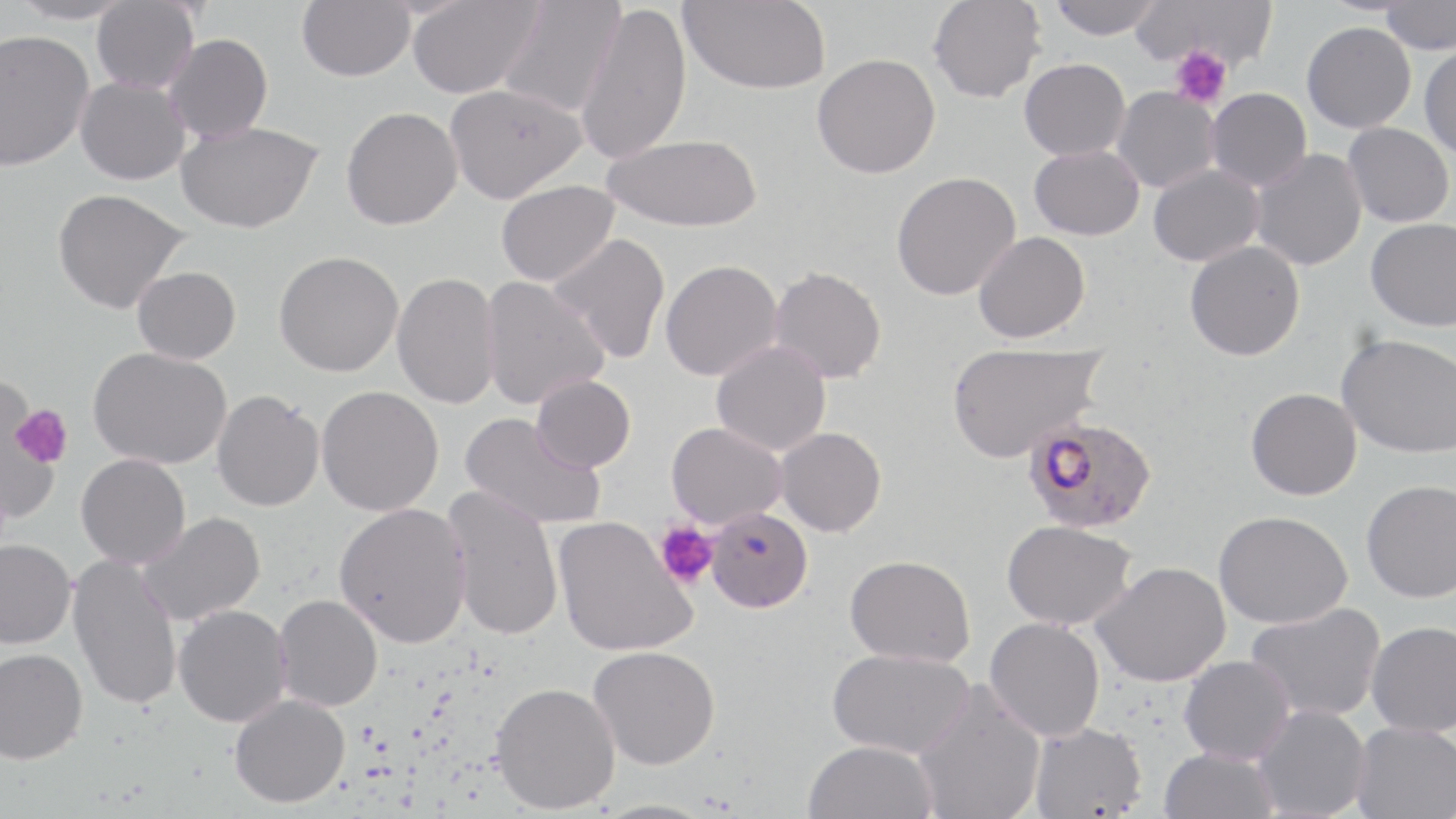
Approximate bounding boxes as named x1/y1/x2/y2 corners in pixels. Uninfected red blood cell locations: (x1=9, y1=0, x2=135, y2=25), (x1=297, y1=0, x2=414, y2=81), (x1=498, y1=0, x2=625, y2=117), (x1=680, y1=0, x2=830, y2=94), (x1=928, y1=0, x2=1045, y2=103), (x1=1047, y1=0, x2=1163, y2=40), (x1=1132, y1=0, x2=1276, y2=68), (x1=1381, y1=0, x2=1456, y2=54), (x1=91, y1=1, x2=199, y2=94), (x1=407, y1=1, x2=542, y2=98), (x1=575, y1=2, x2=691, y2=166), (x1=1301, y1=21, x2=1416, y2=133), (x1=0, y1=29, x2=94, y2=171), (x1=163, y1=34, x2=273, y2=142), (x1=1419, y1=44, x2=1456, y2=160), (x1=811, y1=53, x2=940, y2=179), (x1=1019, y1=58, x2=1130, y2=161), (x1=75, y1=76, x2=190, y2=185), (x1=444, y1=83, x2=585, y2=203), (x1=1111, y1=86, x2=1220, y2=193), (x1=1206, y1=87, x2=1312, y2=191), (x1=341, y1=106, x2=462, y2=230), (x1=175, y1=120, x2=323, y2=233), (x1=1343, y1=122, x2=1454, y2=228), (x1=602, y1=133, x2=763, y2=232), (x1=1029, y1=145, x2=1144, y2=241), (x1=1249, y1=149, x2=1367, y2=271), (x1=1148, y1=164, x2=1264, y2=266), (x1=891, y1=171, x2=1020, y2=300), (x1=496, y1=180, x2=619, y2=286), (x1=52, y1=188, x2=190, y2=313), (x1=1366, y1=218, x2=1456, y2=331), (x1=973, y1=231, x2=1089, y2=343), (x1=548, y1=233, x2=670, y2=364), (x1=1184, y1=240, x2=1305, y2=361), (x1=274, y1=251, x2=403, y2=376), (x1=660, y1=259, x2=783, y2=381), (x1=132, y1=266, x2=240, y2=364), (x1=769, y1=266, x2=887, y2=383), (x1=392, y1=271, x2=501, y2=409), (x1=481, y1=276, x2=609, y2=410), (x1=1336, y1=333, x2=1456, y2=458), (x1=711, y1=340, x2=830, y2=456), (x1=946, y1=341, x2=1105, y2=463), (x1=88, y1=347, x2=232, y2=469), (x1=531, y1=374, x2=635, y2=473), (x1=0, y1=383, x2=62, y2=523), (x1=316, y1=385, x2=443, y2=516), (x1=1245, y1=388, x2=1361, y2=500), (x1=211, y1=389, x2=324, y2=512), (x1=459, y1=411, x2=606, y2=530), (x1=666, y1=422, x2=787, y2=529), (x1=775, y1=427, x2=886, y2=536), (x1=76, y1=454, x2=190, y2=568), (x1=1361, y1=479, x2=1456, y2=603), (x1=442, y1=485, x2=564, y2=640), (x1=334, y1=502, x2=471, y2=648), (x1=706, y1=507, x2=812, y2=613), (x1=1213, y1=510, x2=1352, y2=629), (x1=137, y1=512, x2=265, y2=626), (x1=553, y1=516, x2=696, y2=657), (x1=1001, y1=520, x2=1136, y2=629), (x1=0, y1=538, x2=76, y2=649), (x1=68, y1=554, x2=182, y2=711), (x1=844, y1=554, x2=976, y2=667), (x1=1092, y1=561, x2=1230, y2=686), (x1=273, y1=594, x2=382, y2=711), (x1=1245, y1=602, x2=1386, y2=722), (x1=173, y1=604, x2=292, y2=727), (x1=984, y1=617, x2=1105, y2=741), (x1=1365, y1=620, x2=1456, y2=736), (x1=588, y1=645, x2=719, y2=769), (x1=827, y1=647, x2=975, y2=758), (x1=0, y1=648, x2=87, y2=763), (x1=1179, y1=654, x2=1295, y2=765), (x1=912, y1=680, x2=1046, y2=819), (x1=489, y1=681, x2=620, y2=814), (x1=229, y1=694, x2=350, y2=808), (x1=1253, y1=704, x2=1370, y2=819), (x1=1351, y1=721, x2=1456, y2=819), (x1=1029, y1=722, x2=1147, y2=818), (x1=802, y1=739, x2=938, y2=819), (x1=1159, y1=747, x2=1279, y2=819), (x1=588, y1=798, x2=719, y2=819). Platelet locations: (x1=1170, y1=45, x2=1232, y2=109), (x1=9, y1=403, x2=73, y2=472), (x1=654, y1=521, x2=718, y2=589). Plasmodium falciparum-infected red blood cell locations: (x1=1023, y1=416, x2=1158, y2=533). Slide-level diagnosis: Plasmodium falciparum. 1000x magnification. Thin blood smear. Light microscopy. May-Grünwald-Giemsa stain. Image is 1456×819 pixels. One field of a larger specimen.